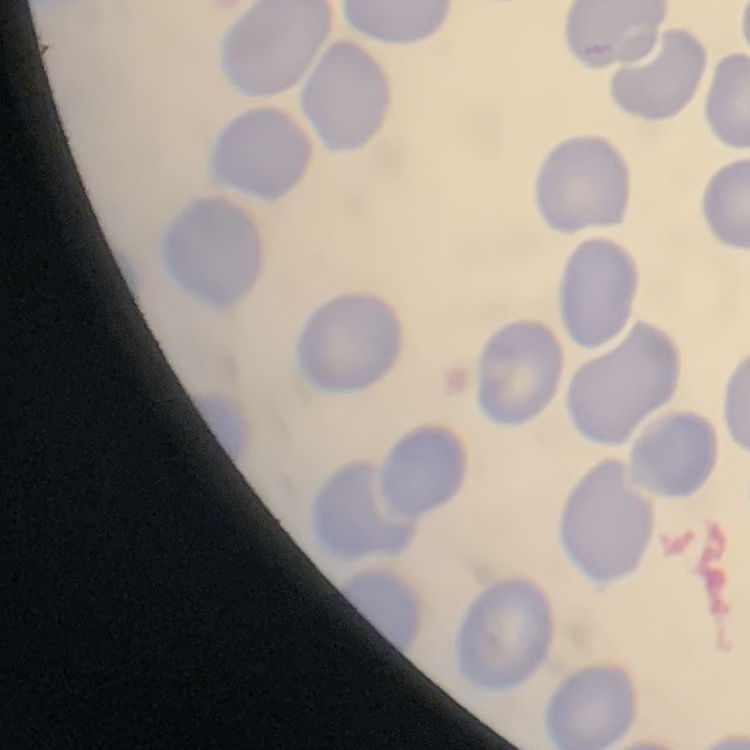

Summary:
  - Erythrocyte morphology: no rouleaux formation
  - Image type: square crop of a larger photomicrograph
  - Preparation: thin blood smear
  - Stain: Field's or Giemsa